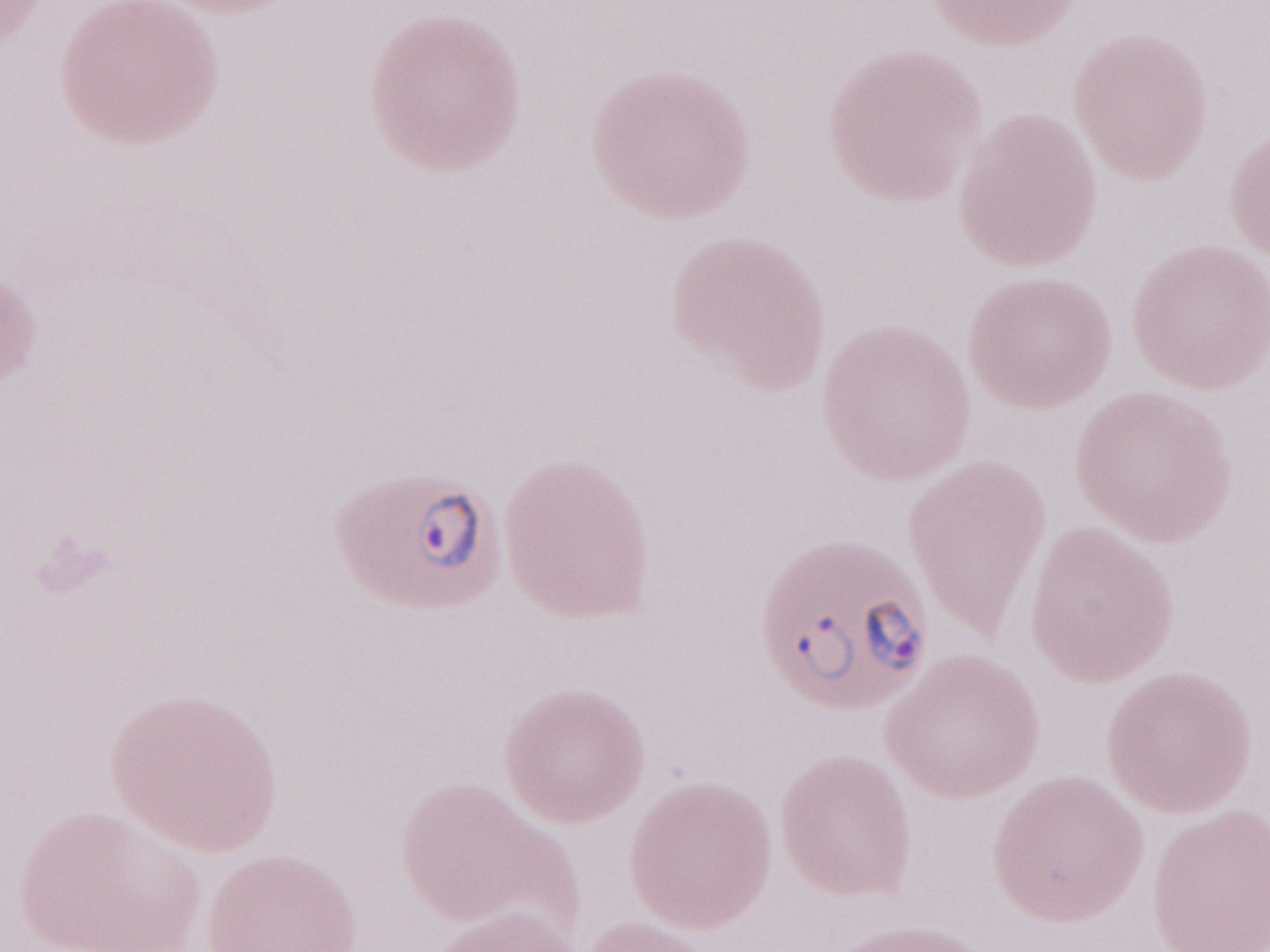
Single field of view. 1,000x magnification. May-Grünwald-Giemsa stain. Image is 1270×952 pixels. Thin peripheral-blood smear. Olympus BX43 microscope, Olympus DP73 camera. Patient-level malaria diagnosis: positive.